State which parasite is depicted.
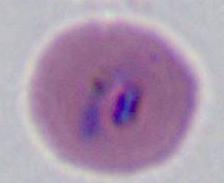

This is Plasmodium.

Micrograph. Captured at either 400x or 1000x magnification.